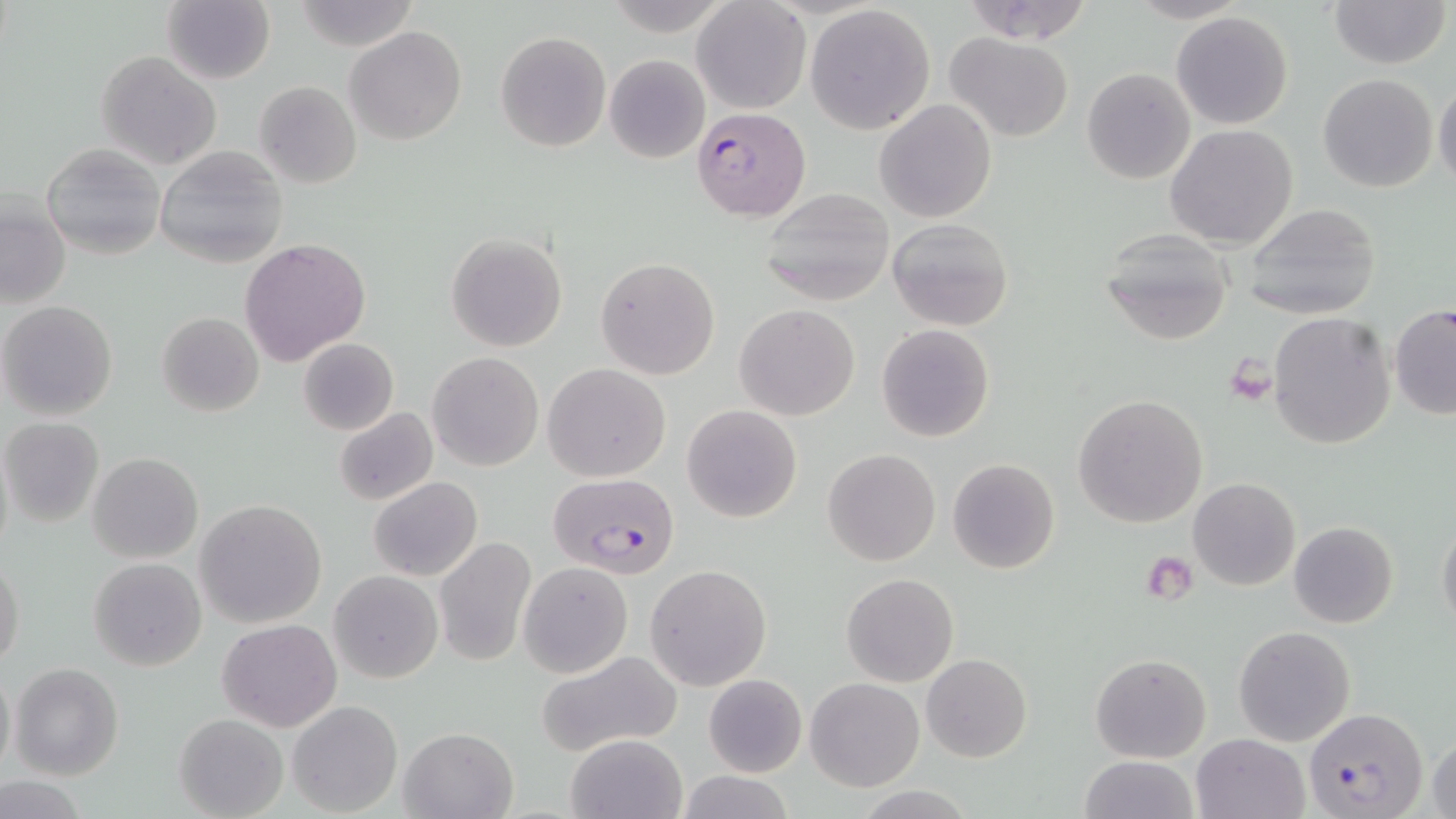 Approximate bounding boxes as [x1, y1, x2, y2] in pixels. Uninfected red blood cell locations: [161, 0, 276, 84], [292, 0, 416, 48], [1328, 0, 1450, 70], [958, 1, 1097, 46], [693, 2, 810, 114], [805, 4, 936, 135], [1171, 10, 1293, 130], [346, 26, 466, 146], [496, 32, 611, 151], [945, 33, 1075, 141], [96, 50, 221, 169], [605, 54, 710, 163], [1082, 67, 1195, 184], [1318, 73, 1438, 192], [1432, 78, 1456, 190], [254, 81, 362, 189], [875, 100, 996, 222], [1164, 123, 1298, 250], [41, 145, 165, 259], [154, 146, 289, 268], [758, 188, 894, 307], [1, 196, 71, 308], [1242, 202, 1382, 319], [886, 218, 1015, 331], [1099, 229, 1236, 347], [446, 233, 567, 353], [239, 238, 370, 364], [596, 257, 721, 380], [0, 301, 118, 421], [736, 303, 858, 421], [1388, 303, 1456, 419], [156, 312, 264, 416], [1269, 312, 1396, 449], [876, 324, 995, 441], [298, 339, 398, 435], [428, 351, 543, 471], [542, 364, 671, 482], [1072, 393, 1207, 528], [681, 404, 802, 522], [333, 407, 439, 507], [0, 418, 104, 527], [0, 437, 14, 564], [823, 448, 941, 566], [88, 453, 203, 564], [947, 458, 1061, 575], [369, 476, 483, 581], [1188, 478, 1300, 590], [196, 499, 327, 627], [1437, 516, 1456, 634], [1288, 521, 1398, 628], [434, 538, 536, 666], [0, 555, 25, 668], [88, 556, 207, 672], [518, 562, 632, 678], [646, 564, 771, 690], [329, 571, 443, 682], [843, 573, 960, 687], [217, 619, 341, 733], [1233, 626, 1357, 747], [535, 649, 684, 759], [921, 653, 1033, 762], [1090, 654, 1211, 761], [1, 663, 15, 778], [11, 663, 124, 781], [703, 673, 806, 777], [806, 677, 925, 791], [288, 701, 403, 816], [174, 712, 287, 818], [400, 727, 517, 819], [1426, 728, 1456, 819], [565, 732, 687, 819], [1191, 733, 1311, 819], [1078, 755, 1200, 819], [678, 771, 793, 819], [0, 777, 88, 816]. Plasmodium falciparum-infected red blood cell locations: [692, 106, 810, 221], [547, 473, 681, 578], [1305, 707, 1429, 819]. Platelet locations: [1225, 356, 1278, 405], [1142, 558, 1197, 609]. Slide-level diagnosis: Plasmodium falciparum. 1000x magnification. Image is 1456×819 pixels. May-Grünwald-Giemsa stain. Optical microscopy. Single field of view. Thin blood smear.